State which cell type is depicted.
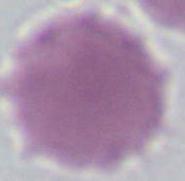

This is an erythrocyte.

Summary:
  - Magnification: 1000x
  - Modality: micrograph